Outline platelets.
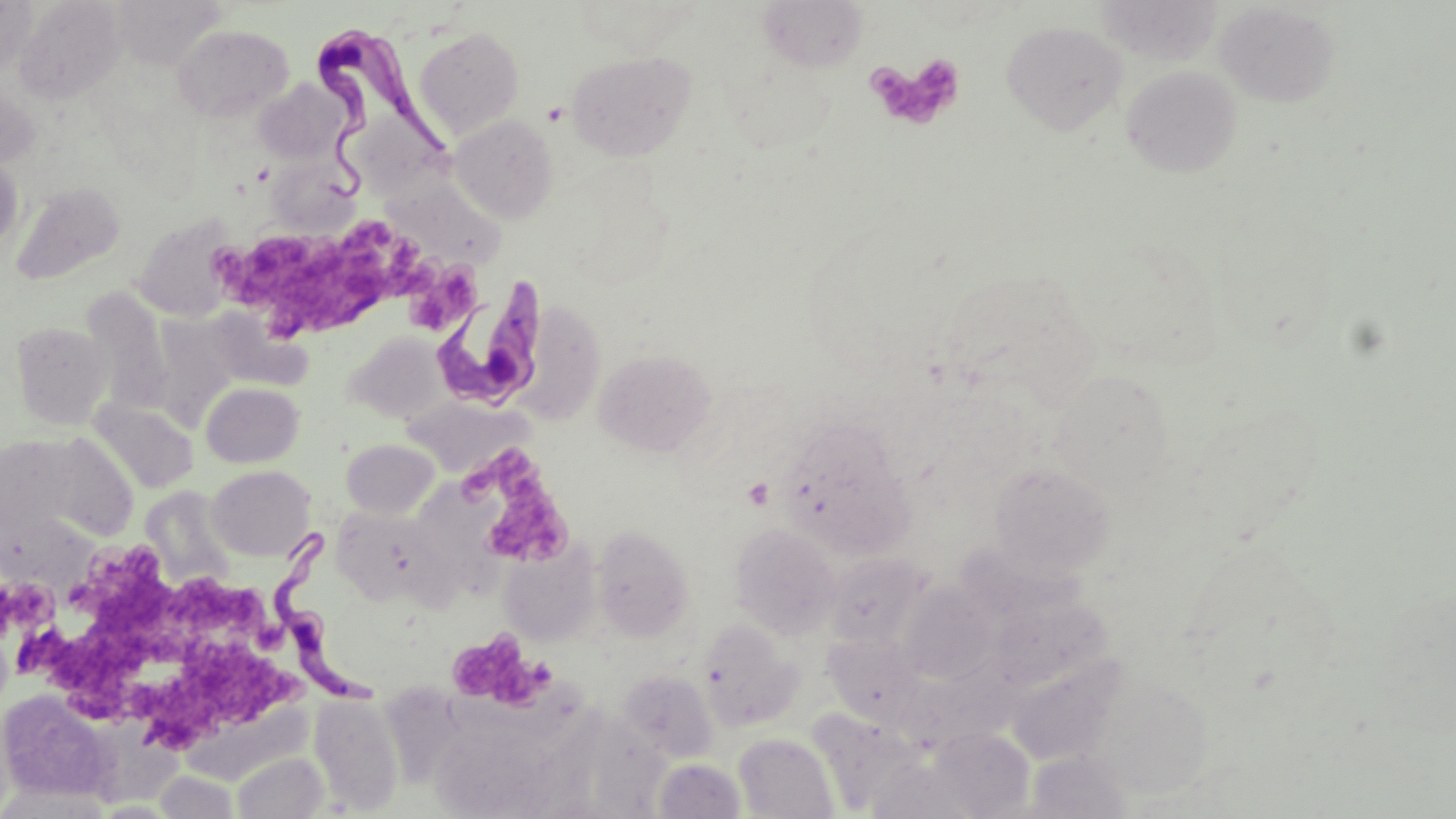
Approximate bounding boxes as [x1, y1, x2, y2] in pixels.
Platelets: [867, 53, 966, 132], [218, 220, 418, 333], [409, 262, 479, 333], [465, 448, 576, 569], [5, 550, 189, 702], [168, 580, 275, 643], [461, 633, 556, 711], [127, 639, 308, 750].

Summary:
  - Trypanosoma brucei locations: [308, 22, 449, 202], [430, 273, 550, 413], [271, 523, 382, 713]
  - Uninfected red blood cell locations: [0, 0, 35, 81], [13, 0, 127, 103], [1096, 0, 1221, 65], [755, 1, 872, 74], [1215, 2, 1341, 108], [1001, 20, 1128, 135], [172, 24, 294, 123], [415, 27, 525, 138], [567, 50, 696, 162], [1122, 65, 1242, 177], [253, 79, 348, 164], [0, 83, 41, 169], [450, 114, 558, 223], [256, 151, 363, 233], [0, 155, 23, 253], [375, 167, 508, 269], [10, 181, 126, 285], [134, 214, 239, 321], [941, 268, 1098, 402], [80, 288, 173, 414], [517, 300, 605, 424], [11, 322, 114, 429], [348, 332, 450, 423], [594, 348, 717, 457], [1049, 369, 1174, 497], [201, 381, 304, 468], [404, 397, 529, 477], [88, 398, 198, 494], [778, 423, 915, 558], [16, 430, 140, 549], [341, 439, 440, 518], [988, 462, 1116, 578], [207, 465, 315, 560], [133, 486, 232, 588], [330, 506, 453, 617], [730, 522, 841, 640], [593, 524, 694, 641], [498, 539, 601, 646], [825, 552, 931, 650], [898, 583, 999, 683], [988, 595, 1113, 693], [698, 619, 805, 731], [824, 634, 927, 728], [1005, 658, 1123, 765], [619, 669, 718, 764], [1086, 676, 1215, 800], [1, 689, 119, 806], [188, 690, 324, 780], [309, 694, 404, 814], [425, 694, 597, 816], [95, 716, 184, 802], [929, 727, 1036, 818], [733, 733, 839, 818], [1025, 750, 1134, 818], [231, 751, 329, 818], [654, 758, 746, 818], [152, 770, 240, 818]
  - Slide-level diagnosis: Trypanosoma brucei
  - Modality: optical microscopy
  - Magnification: 1000x
  - Image size: 1456×819 pixels
  - Field of view: single
  - Stain: May-Grünwald-Giemsa
  - Preparation: thin blood smear